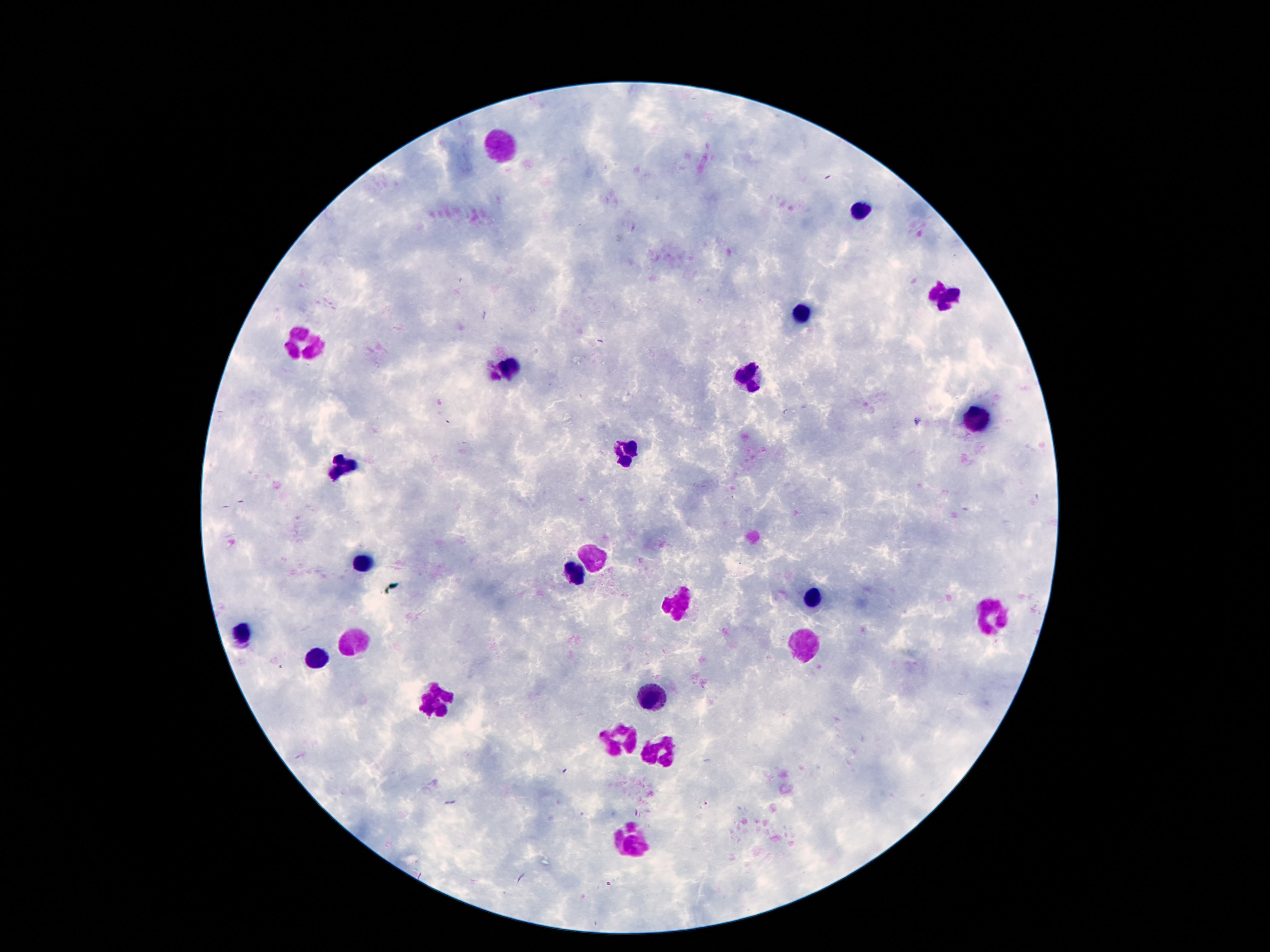

patient malaria status = uninfected
field of view = single
image size = 1270×952 pixels
preparation = thick blood smear
stain = Giemsa
capture = smartphone camera through the microscope eyepiece
magnification = 100x
leukocyte locations = approximate centers as [x, y] in pixels: [505, 145], [862, 210], [939, 294], [803, 310], [305, 342], [510, 369], [753, 378], [969, 419], [626, 453], [337, 465], [591, 559], [367, 564], [573, 569], [678, 601], [814, 601], [998, 618], [242, 630], [805, 639], [353, 641], [317, 658], [437, 696], [650, 696], [619, 736], [662, 757], [632, 839]